Assess the morphology of the erythrocytes.
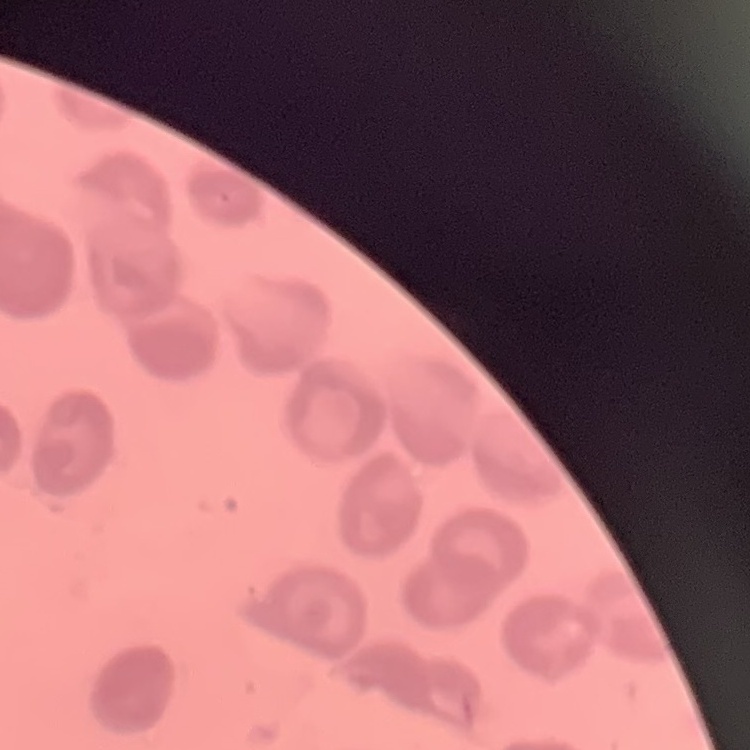

They show no rouleaux formation.

preparation = thin blood film
stain = Field's or Giemsa
image type = one tile cut from a larger photomicrograph